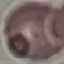

result: no malaria parasites detected
capture: smartphone camera at the microscope eyepiece
preparation: thin smear
image_type: cell patch, automatically extracted from a larger field of view and resized to 64 × 64 pixels
stain: Giemsa